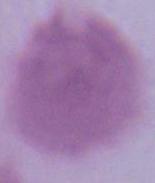

identification: erythrocyte
magnification: 1000x
modality: micrograph